Describe the morphology of the red blood cells.
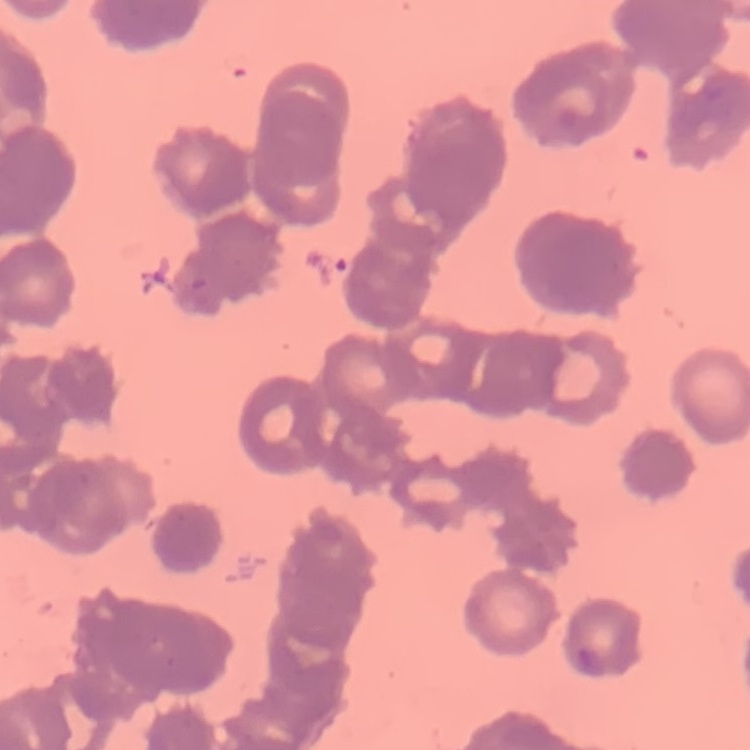

Rouleaux formation.

Stained with either Field's or Giemsa. Thin blood film. One tile cut from a larger photomicrograph.